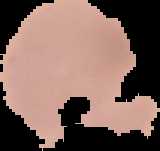
preparation = thin blood smear
image type = segmented cell region on a black background
image size = 160×151 pixels
malaria status = uninfected